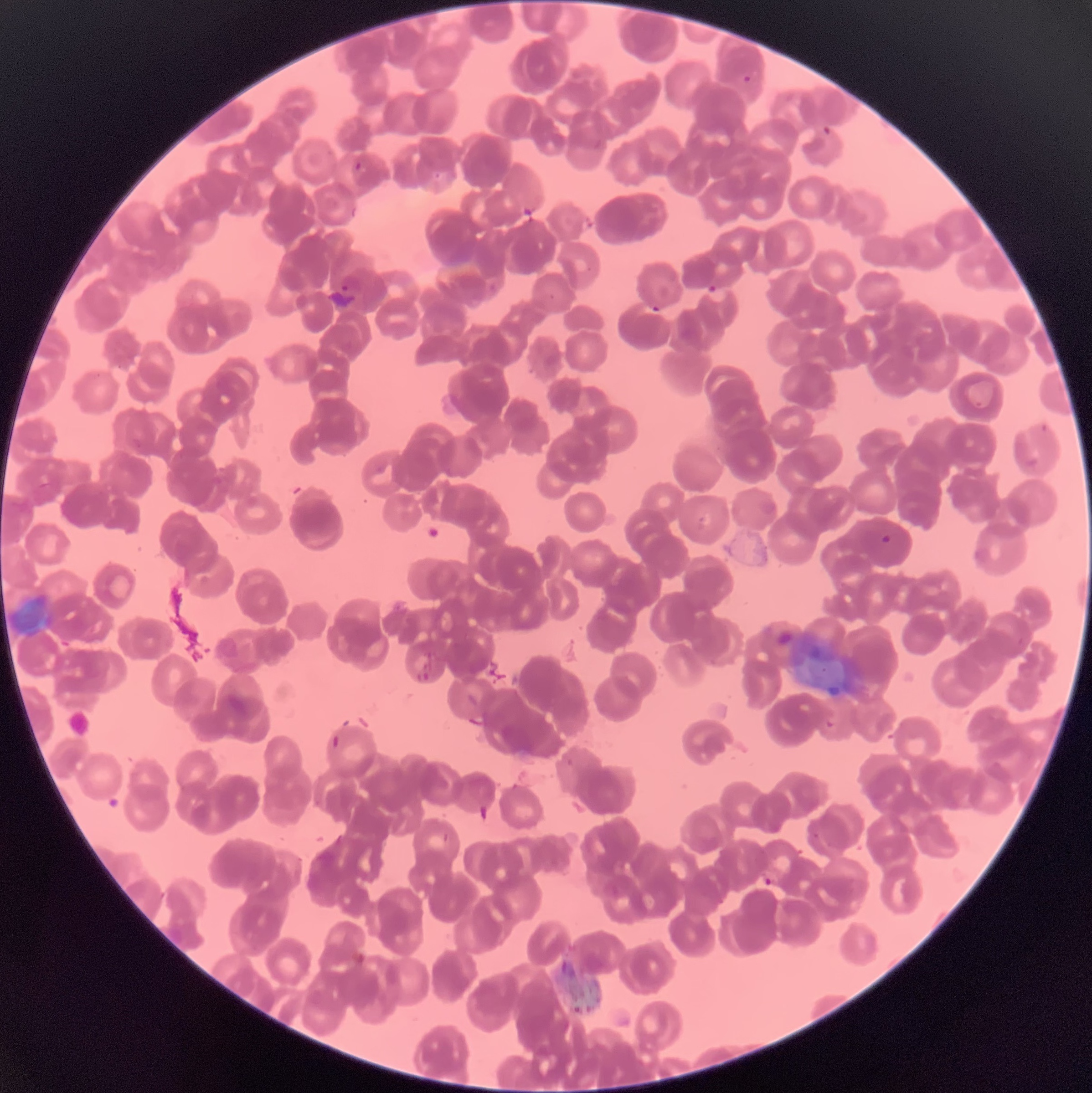
Approximate bounding boxes as (x1, y1, x2, y2) in pixels. Plasmodium parasite locations: (742, 75, 751, 83), (823, 126, 832, 135), (355, 162, 362, 171), (341, 275, 364, 293), (705, 285, 729, 302), (646, 305, 663, 316), (1041, 423, 1051, 435), (130, 438, 143, 451), (880, 533, 893, 544), (824, 716, 837, 728), (760, 869, 781, 888). Optical microscopy. The red blood cells show rouleaux formation. Thin blood smear. Image is 1092×1093 pixels.